Outline each blood parasite and name the species.
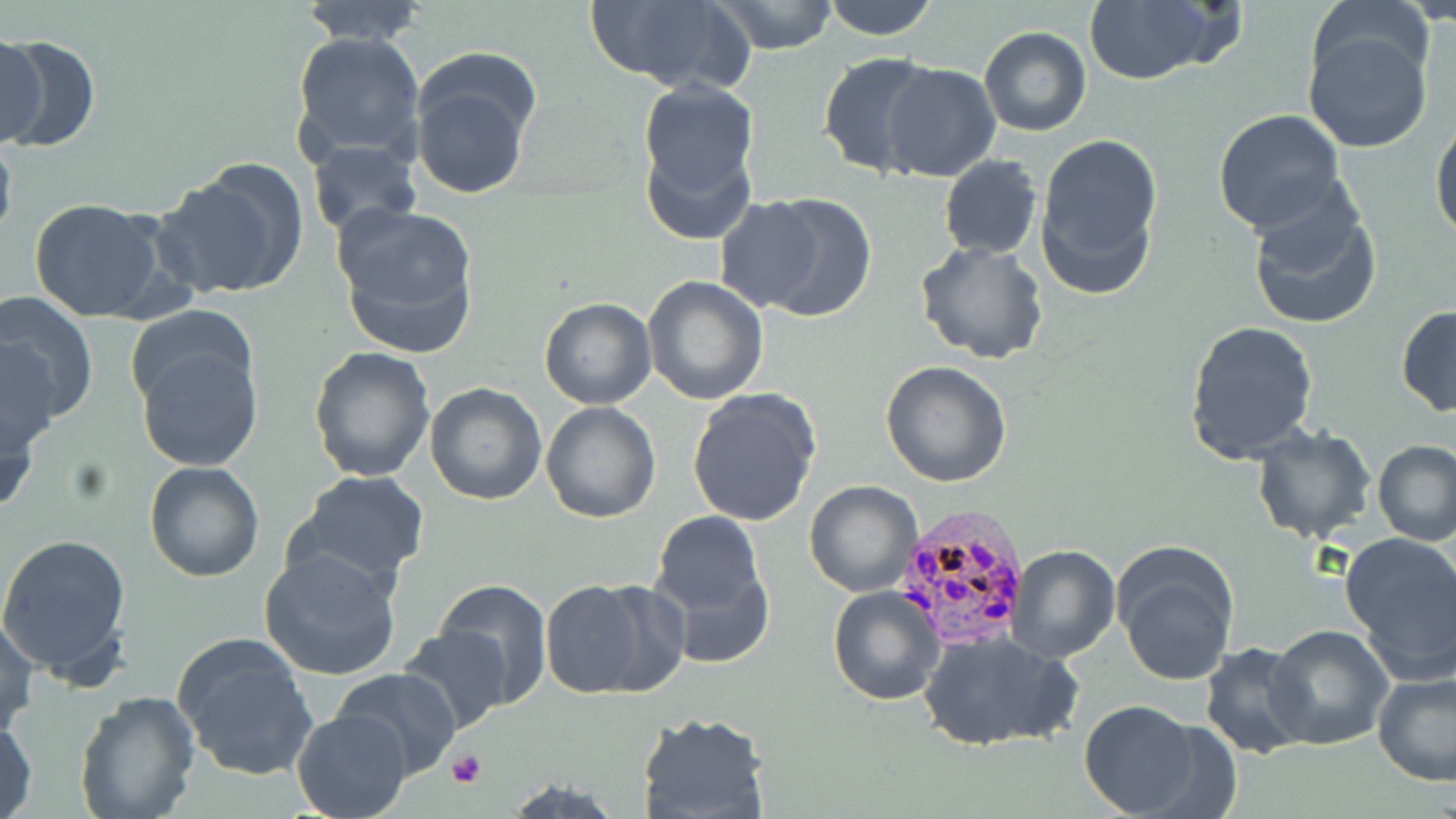

Approximate bounding boxes as named x1/y1/x2/y2 corners in pixels.
Plasmodium ovale-infected red blood cells: (x1=892, y1=505, x2=1030, y2=653).
No Plasmodium falciparum, Plasmodium malariae, Plasmodium vivax, Babesia divergens, or Trypanosoma brucei observed.

Uninfected red blood cell locations: (x1=296, y1=0, x2=430, y2=46), (x1=586, y1=0, x2=753, y2=94), (x1=713, y1=0, x2=842, y2=54), (x1=820, y1=0, x2=940, y2=40), (x1=1309, y1=0, x2=1435, y2=97), (x1=1082, y1=1, x2=1229, y2=86), (x1=978, y1=26, x2=1091, y2=136), (x1=1301, y1=26, x2=1432, y2=154), (x1=290, y1=29, x2=426, y2=169), (x1=0, y1=33, x2=100, y2=153), (x1=0, y1=37, x2=46, y2=145), (x1=818, y1=50, x2=944, y2=177), (x1=411, y1=55, x2=540, y2=200), (x1=880, y1=63, x2=1002, y2=183), (x1=635, y1=78, x2=761, y2=202), (x1=1212, y1=108, x2=1345, y2=238), (x1=1430, y1=112, x2=1456, y2=248), (x1=0, y1=130, x2=18, y2=249), (x1=1035, y1=132, x2=1165, y2=296), (x1=641, y1=137, x2=756, y2=245), (x1=308, y1=140, x2=422, y2=236), (x1=938, y1=156, x2=1042, y2=259), (x1=155, y1=159, x2=309, y2=301), (x1=1245, y1=181, x2=1383, y2=333), (x1=747, y1=193, x2=878, y2=322), (x1=715, y1=195, x2=824, y2=312), (x1=27, y1=198, x2=173, y2=323), (x1=331, y1=205, x2=481, y2=357), (x1=916, y1=241, x2=1049, y2=364), (x1=642, y1=276, x2=769, y2=407), (x1=0, y1=293, x2=99, y2=433), (x1=537, y1=296, x2=656, y2=409), (x1=124, y1=304, x2=259, y2=411), (x1=1395, y1=305, x2=1456, y2=416), (x1=1186, y1=320, x2=1319, y2=467), (x1=0, y1=337, x2=58, y2=455), (x1=137, y1=341, x2=262, y2=472), (x1=308, y1=347, x2=436, y2=483), (x1=880, y1=360, x2=1012, y2=487), (x1=423, y1=382, x2=547, y2=504), (x1=686, y1=387, x2=821, y2=528), (x1=0, y1=392, x2=42, y2=518), (x1=541, y1=400, x2=661, y2=524), (x1=1251, y1=423, x2=1377, y2=544), (x1=1372, y1=438, x2=1455, y2=548), (x1=144, y1=461, x2=264, y2=583), (x1=288, y1=471, x2=431, y2=586), (x1=804, y1=481, x2=924, y2=598), (x1=648, y1=510, x2=770, y2=651), (x1=0, y1=531, x2=134, y2=686), (x1=1341, y1=532, x2=1456, y2=679), (x1=1006, y1=544, x2=1120, y2=663), (x1=259, y1=546, x2=405, y2=680), (x1=1113, y1=546, x2=1238, y2=687), (x1=437, y1=577, x2=553, y2=705), (x1=540, y1=579, x2=682, y2=700), (x1=827, y1=584, x2=944, y2=704), (x1=0, y1=615, x2=38, y2=737), (x1=398, y1=624, x2=512, y2=734), (x1=1267, y1=625, x2=1395, y2=751), (x1=170, y1=630, x2=319, y2=782), (x1=919, y1=632, x2=1079, y2=752), (x1=1199, y1=642, x2=1314, y2=758), (x1=330, y1=668, x2=463, y2=780), (x1=1371, y1=670, x2=1456, y2=785), (x1=72, y1=692, x2=202, y2=819), (x1=1080, y1=700, x2=1204, y2=816), (x1=291, y1=709, x2=412, y2=818), (x1=637, y1=711, x2=770, y2=819), (x1=0, y1=713, x2=38, y2=819), (x1=502, y1=777, x2=629, y2=818). Platelet locations: (x1=447, y1=749, x2=487, y2=787). Slide-level diagnosis: Plasmodium ovale. May-Grünwald-Giemsa-stained preparation. 1000x magnification. Optical microscopy. Single field of view. Thin blood smear. Image is 1456×819 pixels.